Name the parasite shown.
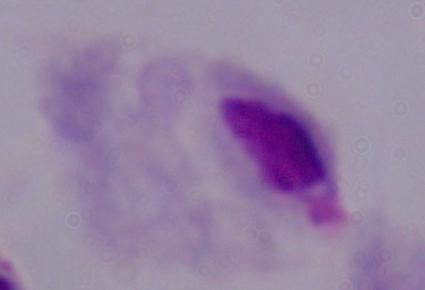
This is a trichomonad.

Micrograph. Captured at 1000x magnification.